Identify the parasite.
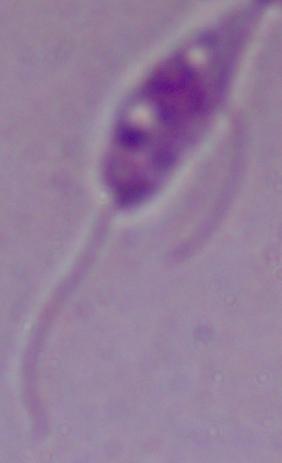
This is Leishmania.

Summary:
  - Modality: micrograph
  - Magnification: 1000x